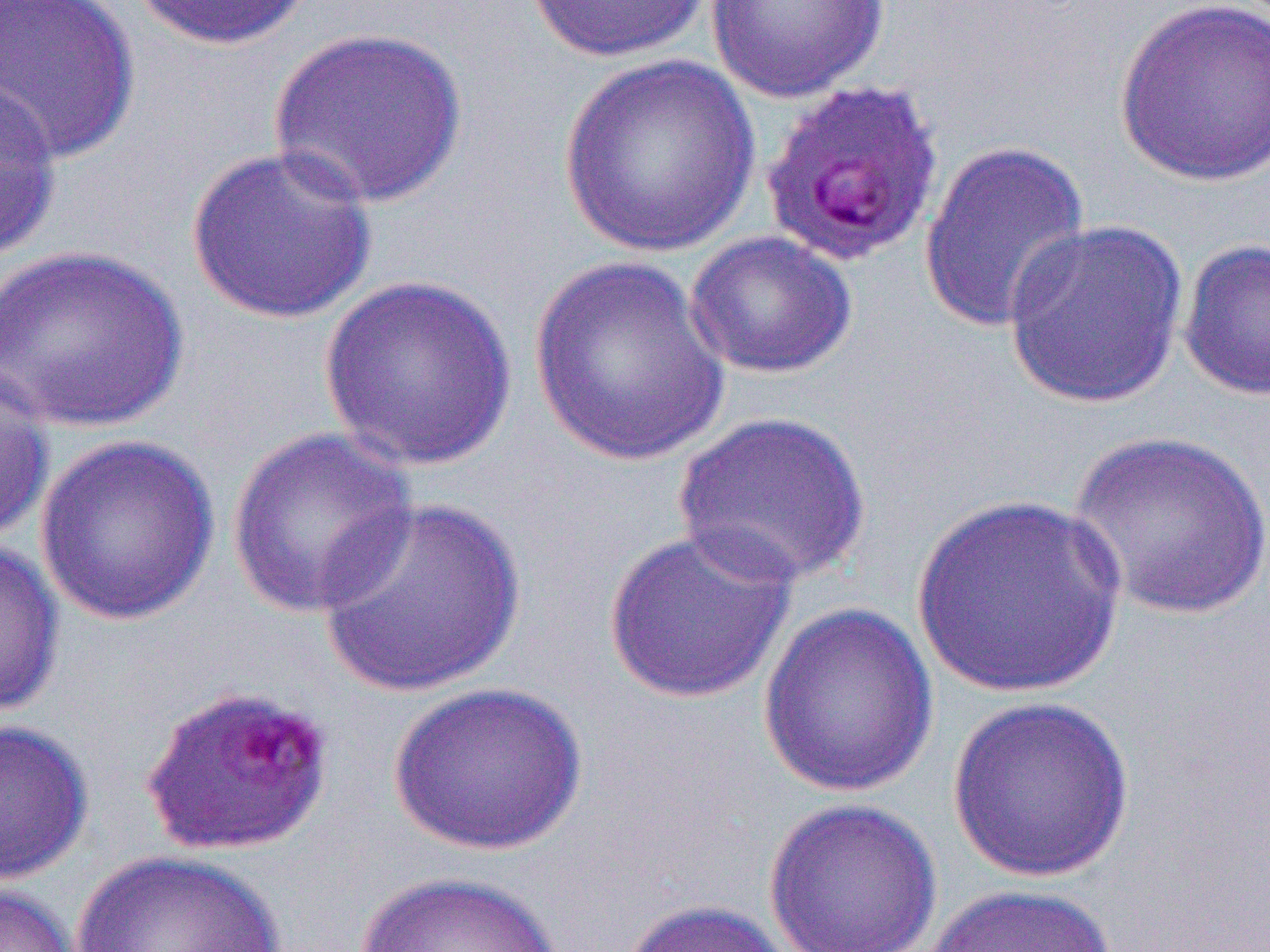

Summary:
  - Coordinate format: approximate bounding boxes as (x1,y1)-(x2,y2) corner pairs in pixels
  - Uninfected red blood cell locations: (0,0)-(140,165), (132,0)-(317,51), (524,0)-(717,63), (705,0)-(891,103), (1114,0)-(1270,187), (268,27)-(468,209), (558,54)-(762,258), (1,73)-(63,262), (918,139)-(1092,335), (185,144)-(379,325), (1001,217)-(1191,409), (684,231)-(858,379), (1178,237)-(1270,402), (0,244)-(190,434), (528,257)-(732,465), (319,275)-(519,470), (0,364)-(55,543), (672,410)-(872,587), (226,425)-(420,618), (1067,429)-(1270,621), (33,433)-(221,627), (912,493)-(1129,699), (316,494)-(527,697), (602,525)-(799,705), (0,536)-(64,720), (757,601)-(939,800), (389,681)-(587,856), (946,694)-(1136,883), (0,719)-(94,884), (762,797)-(944,952), (72,850)-(293,952), (353,870)-(562,952), (0,883)-(83,952), (920,883)-(1118,952), (615,898)-(806,952)
  - Slide-level diagnosis: Plasmodium falciparum
  - Image size: 1270×952 pixels
  - Field of view: one of a larger specimen
  - Modality: optical microscopy
  - Magnification: 1000x
  - Preparation: thin blood film